State which parasite is depicted.
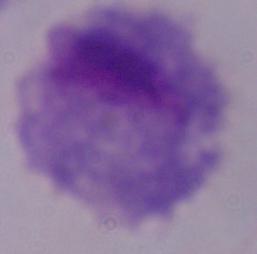

A trichomonad.

Summary:
  - Modality: photomicrograph
  - Magnification: 1000x